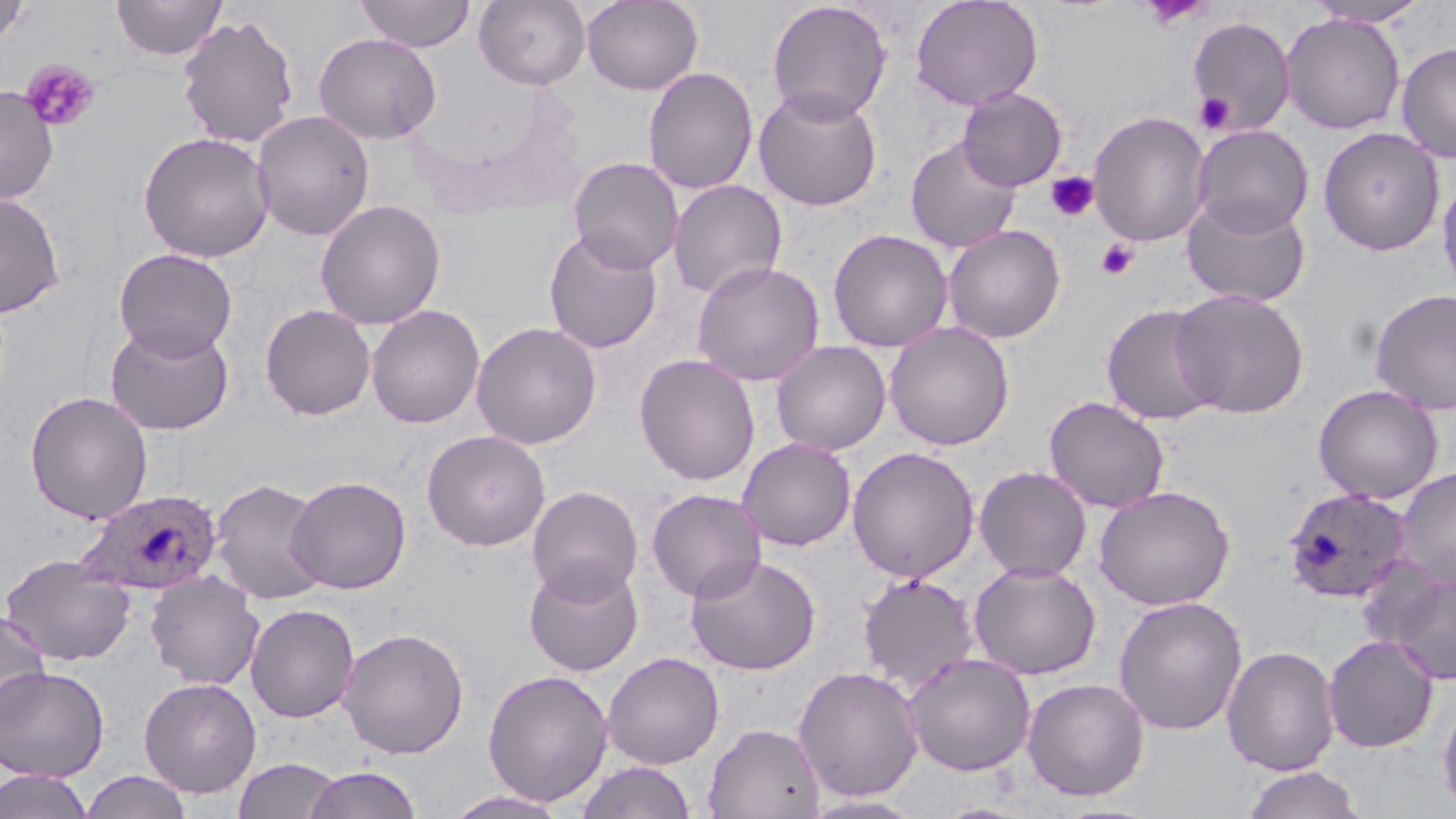

Summary:
  - Coordinate format: approximate bounding boxes as named x1/y1/x2/y2 corners in pixels
  - Platelet locations: (x1=1138, y1=0, x2=1215, y2=30), (x1=21, y1=59, x2=100, y2=132), (x1=1194, y1=92, x2=1236, y2=135), (x1=1046, y1=171, x2=1099, y2=222), (x1=1096, y1=238, x2=1140, y2=280)
  - Plasmodium ovale-infected red blood cell locations: (x1=1282, y1=487, x2=1412, y2=602), (x1=74, y1=489, x2=223, y2=596)
  - Uninfected red blood cell locations: (x1=112, y1=0, x2=226, y2=60), (x1=355, y1=0, x2=476, y2=52), (x1=475, y1=0, x2=590, y2=89), (x1=581, y1=0, x2=704, y2=95), (x1=910, y1=0, x2=1044, y2=111), (x1=0, y1=1, x2=31, y2=50), (x1=766, y1=1, x2=892, y2=124), (x1=1138, y1=1, x2=1216, y2=28), (x1=1304, y1=1, x2=1430, y2=27), (x1=1280, y1=13, x2=1406, y2=134), (x1=177, y1=14, x2=300, y2=148), (x1=1186, y1=15, x2=1296, y2=136), (x1=314, y1=33, x2=442, y2=145), (x1=1395, y1=42, x2=1456, y2=163), (x1=643, y1=67, x2=759, y2=195), (x1=0, y1=85, x2=59, y2=205), (x1=753, y1=86, x2=883, y2=212), (x1=957, y1=87, x2=1068, y2=191), (x1=252, y1=110, x2=375, y2=241), (x1=1088, y1=110, x2=1212, y2=248), (x1=1192, y1=124, x2=1314, y2=237), (x1=1317, y1=126, x2=1444, y2=255), (x1=138, y1=131, x2=274, y2=262), (x1=905, y1=137, x2=1022, y2=253), (x1=567, y1=156, x2=684, y2=274), (x1=1437, y1=169, x2=1456, y2=302), (x1=668, y1=180, x2=787, y2=300), (x1=0, y1=191, x2=65, y2=317), (x1=1181, y1=195, x2=1312, y2=308), (x1=314, y1=198, x2=447, y2=330), (x1=943, y1=224, x2=1066, y2=344), (x1=542, y1=227, x2=664, y2=354), (x1=828, y1=228, x2=953, y2=353), (x1=113, y1=247, x2=238, y2=360), (x1=691, y1=260, x2=825, y2=386), (x1=1369, y1=288, x2=1456, y2=414), (x1=1170, y1=289, x2=1310, y2=419), (x1=260, y1=303, x2=376, y2=421), (x1=1101, y1=304, x2=1223, y2=427), (x1=366, y1=305, x2=485, y2=429), (x1=105, y1=319, x2=235, y2=436), (x1=471, y1=321, x2=602, y2=450), (x1=883, y1=321, x2=1015, y2=451), (x1=770, y1=340, x2=892, y2=455), (x1=633, y1=353, x2=761, y2=486), (x1=1313, y1=384, x2=1444, y2=504), (x1=24, y1=391, x2=153, y2=524), (x1=1044, y1=396, x2=1170, y2=513), (x1=421, y1=429, x2=551, y2=550), (x1=737, y1=438, x2=857, y2=551), (x1=846, y1=446, x2=981, y2=583), (x1=974, y1=465, x2=1093, y2=581), (x1=1395, y1=467, x2=1456, y2=590), (x1=285, y1=475, x2=412, y2=595), (x1=209, y1=477, x2=331, y2=605), (x1=526, y1=485, x2=643, y2=603), (x1=1094, y1=485, x2=1235, y2=610), (x1=646, y1=488, x2=766, y2=603), (x1=1, y1=553, x2=134, y2=666), (x1=685, y1=553, x2=822, y2=675), (x1=523, y1=559, x2=644, y2=677), (x1=968, y1=561, x2=1102, y2=679), (x1=1383, y1=570, x2=1456, y2=685), (x1=145, y1=571, x2=265, y2=690), (x1=857, y1=572, x2=979, y2=693), (x1=1113, y1=596, x2=1248, y2=736), (x1=245, y1=603, x2=360, y2=723), (x1=0, y1=607, x2=51, y2=730), (x1=337, y1=627, x2=470, y2=759), (x1=1322, y1=634, x2=1439, y2=753), (x1=1222, y1=644, x2=1340, y2=776), (x1=602, y1=652, x2=724, y2=769), (x1=903, y1=652, x2=1036, y2=776), (x1=0, y1=664, x2=110, y2=782), (x1=792, y1=665, x2=925, y2=802), (x1=482, y1=668, x2=614, y2=808), (x1=139, y1=677, x2=262, y2=798), (x1=1021, y1=677, x2=1150, y2=801), (x1=1437, y1=694, x2=1456, y2=818), (x1=703, y1=722, x2=826, y2=819), (x1=232, y1=756, x2=343, y2=818), (x1=573, y1=760, x2=698, y2=819), (x1=1240, y1=765, x2=1368, y2=819), (x1=303, y1=766, x2=424, y2=818), (x1=0, y1=770, x2=95, y2=819), (x1=79, y1=770, x2=195, y2=819), (x1=441, y1=790, x2=572, y2=818), (x1=799, y1=794, x2=928, y2=818)
  - Slide-level diagnosis: Plasmodium ovale
  - Field of view: single
  - Stain: May-Grünwald-Giemsa
  - Magnification: 1000x
  - Image size: 1456×819 pixels
  - Preparation: thin blood film
  - Modality: light microscopy